Describe the morphology of the erythrocytes.
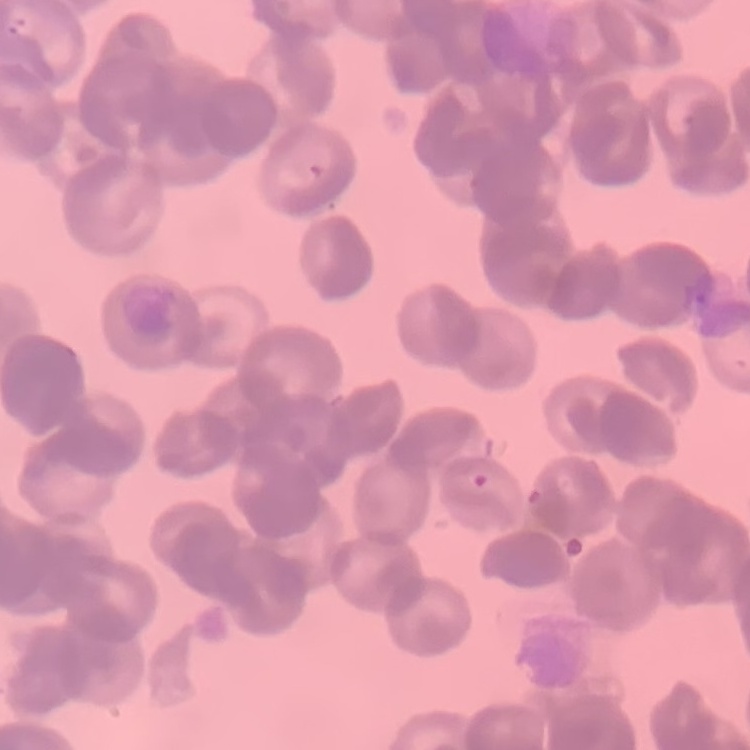
They show rouleaux formation.

preparation = thin blood film
stain = Field's or Giemsa
image type = square crop of a larger photomicrograph